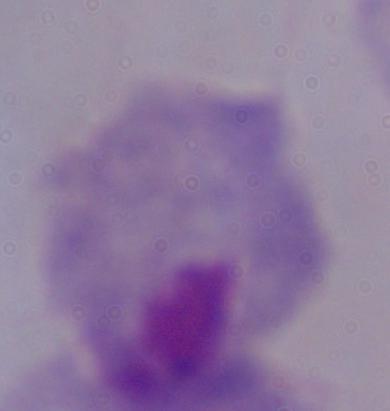
modality = micrograph
identification = trichomonad
magnification = 1000x